Give the position of every P. falciparum parasite, noting its life-cycle stage.
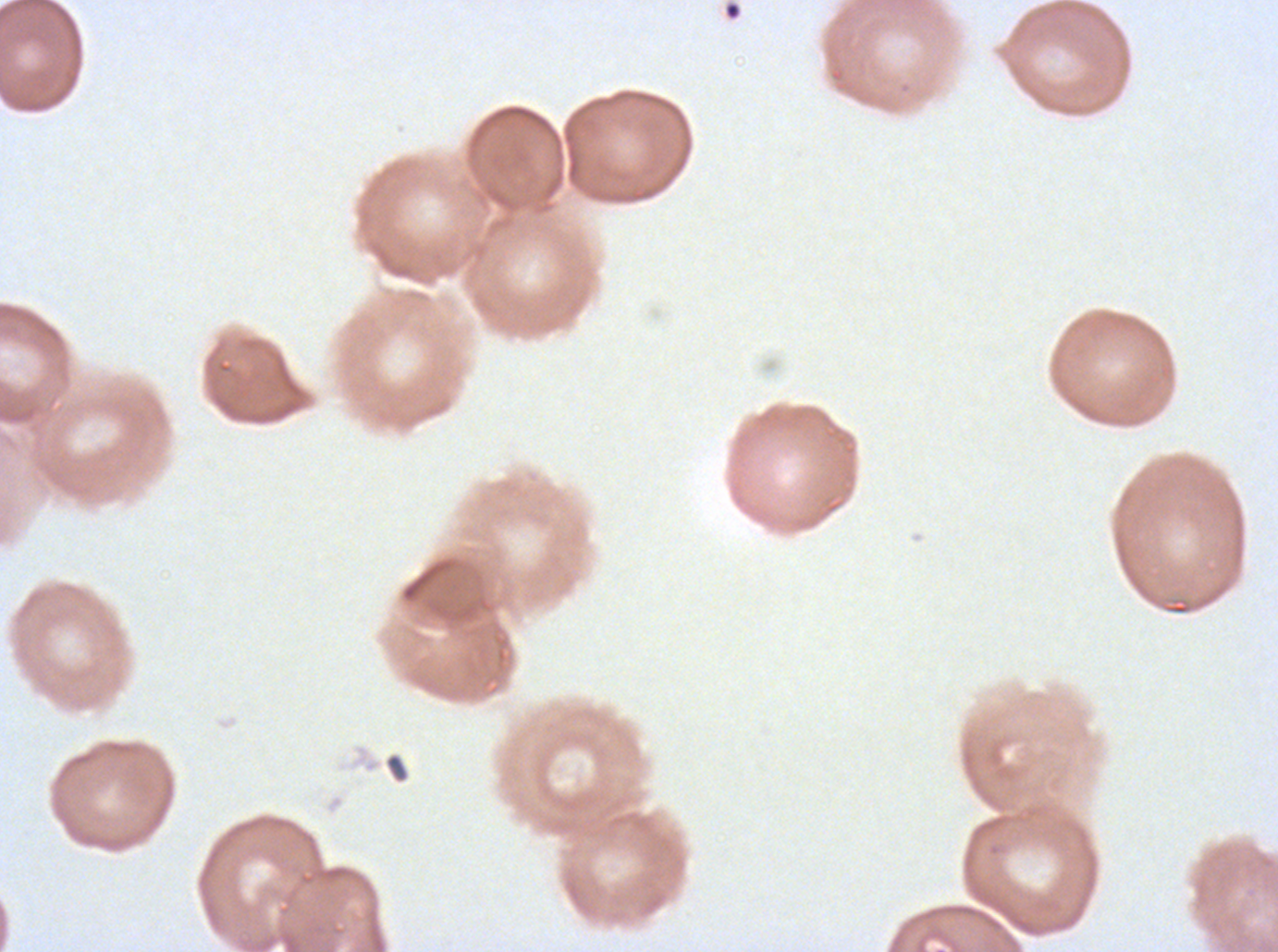

No rings, late-ring/early-trophozoite forms, mid trophozoites, late trophozoites, early schizonts, late schizonts, segmenters, or gametocytes observed.

notation = approximate bounding boxes as [x1, y1, x2, y2] in pixels
debris locations = [384, 752, 410, 784]
image size = 1278×952 pixels
specimen = P. falciparum from a patient in The Gambia, cultured ex vivo for 24 to 48 hours
field of view = sub-image separated from a larger composite
preparation = thin blood smear
stain = Giemsa